Give the preparation type.
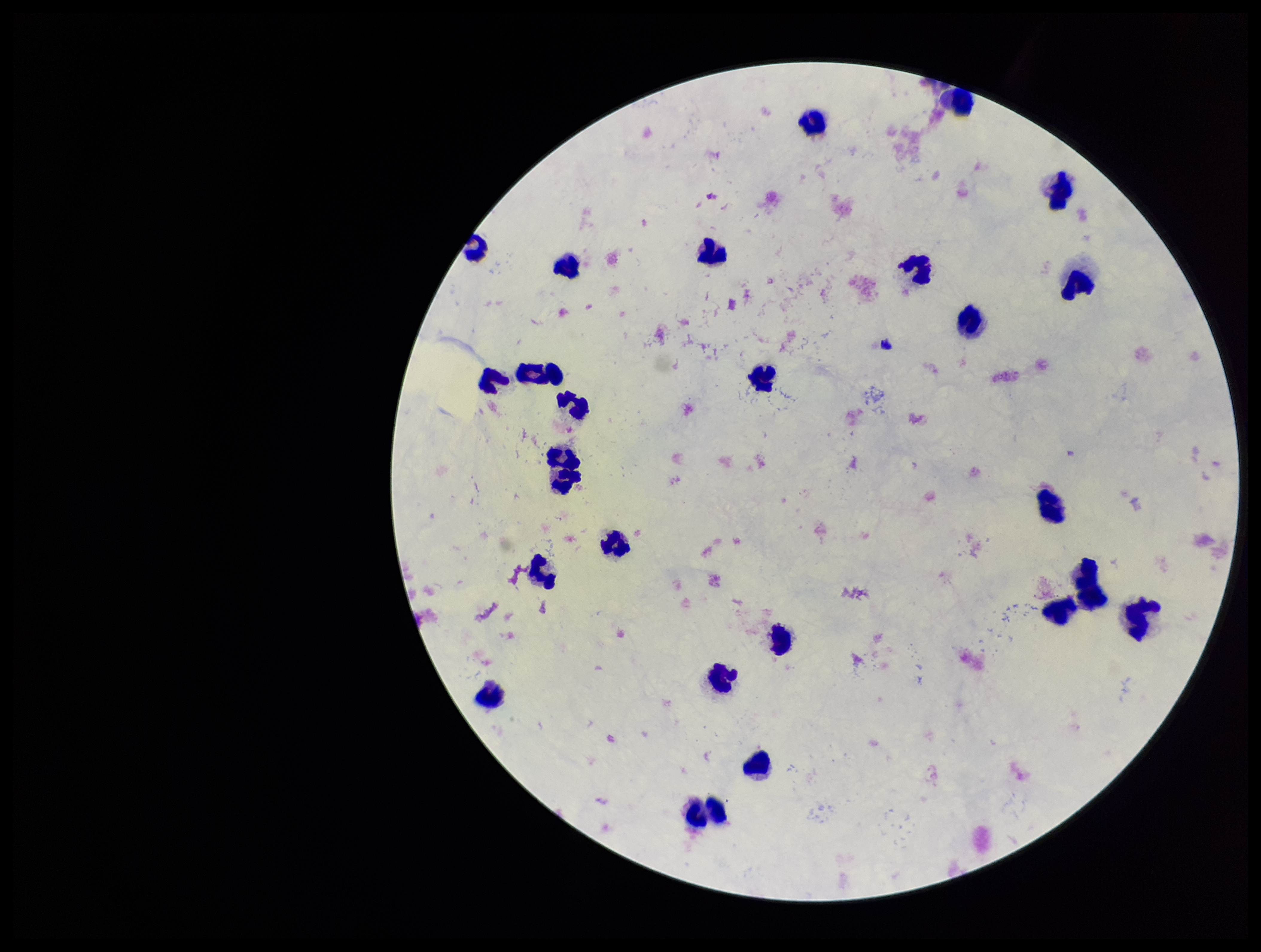

Thick.

Summary:
  - Field of view: single
  - Capture: smartphone photograph through the microscope eyepiece
  - Image size: 1261×952 pixels
  - Parasite count: 0
  - Stain: Giemsa
  - Patient malaria status: negative
  - Plasmodium parasites: none detected
  - Leukocyte count: 25